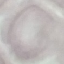

{
  "result": "no malaria parasites seen",
  "preparation": "thin blood film",
  "image_type": "cell patch, automatically extracted from a larger field of view and resized to 64 × 64 pixels",
  "capture": "smartphone camera at the microscope eyepiece",
  "stain": "Giemsa"
}